Assess this cell for malaria.
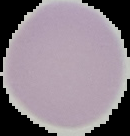
Uninfected.

image size = 130×136 pixels
preparation = thin blood smear
image type = cell region segmented out of the field of view; surrounding area masked to black